Identify the parasite.
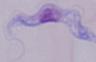
This is a trypanosome.

Photomicrograph. Captured at 1000x magnification.